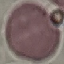

Malaria status: uninfected. Automatically extracted cell patch, resized to 64 × 64 pixels. Thin blood film. Giemsa stain. Photographed with a smartphone camera at the microscope eyepiece.